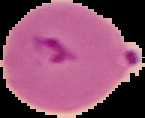

image size = 145×118 pixels
image type = cell region segmented out of the field of view; surrounding area masked to black
result = Plasmodium parasites identified
preparation = thin blood film